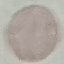

Summary:
  - Result: negative for malaria parasites
  - Stain: Giemsa
  - Preparation: thin blood smear
  - Image type: cell patch, automatically extracted from a larger field of view and resized to 64 × 64 pixels
  - Capture: smartphone through the microscope eyepiece